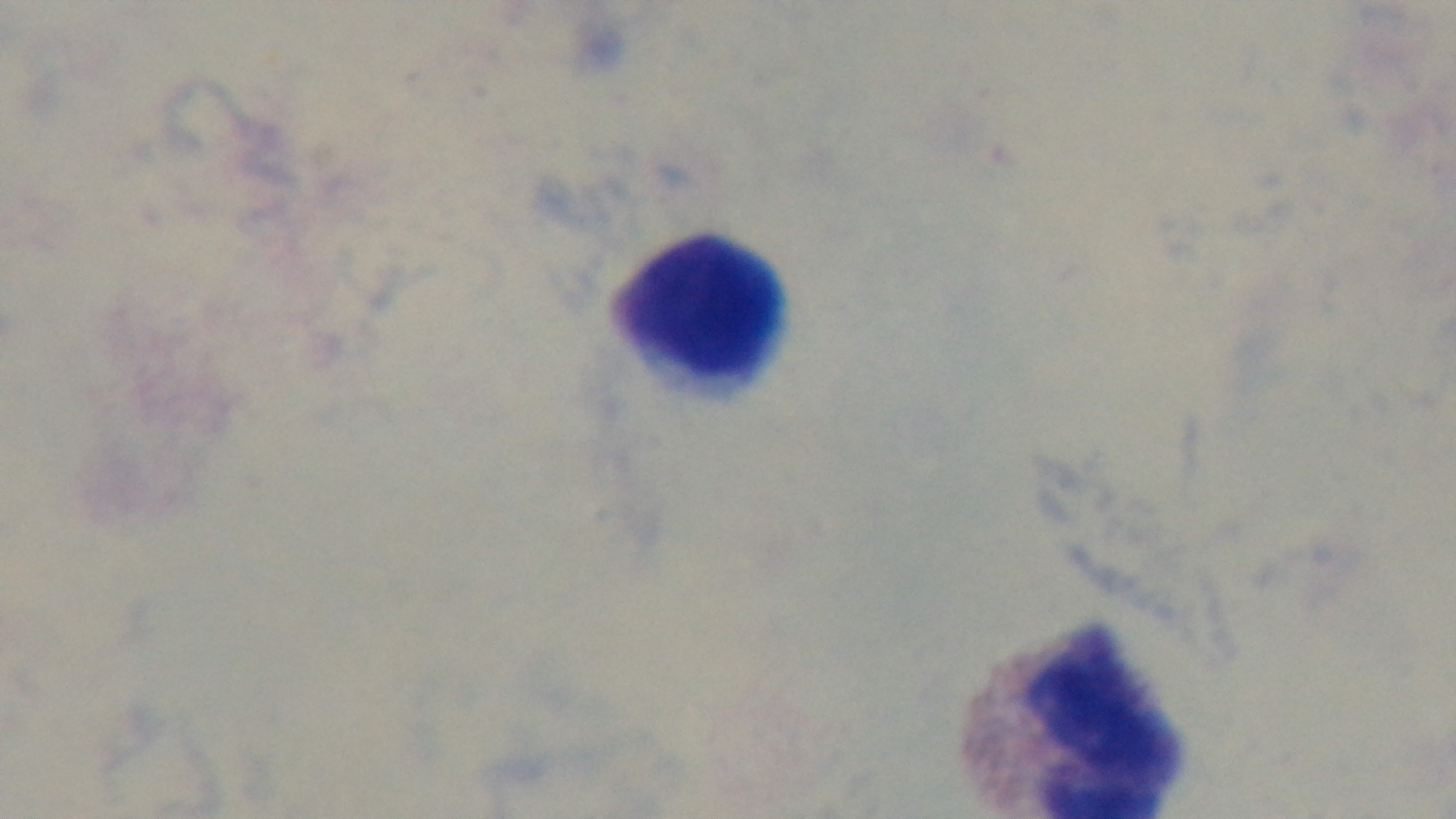
Single field of view. Malaria status: negative. Mounted 4K digital camera. 100x oil-immersion objective. Preparation: thick. Light microscopy. Giemsa-stained.